Name the cell type shown.
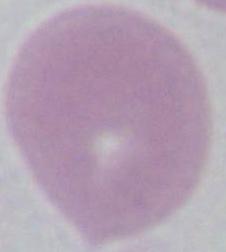

An erythrocyte.

Summary:
  - Modality: photomicrograph
  - Magnification: 1000x